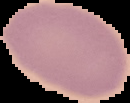
image size = 130×103 pixels
result = no malaria parasites seen
preparation = thin blood smear
image type = segmented cell region with the area outside set to black